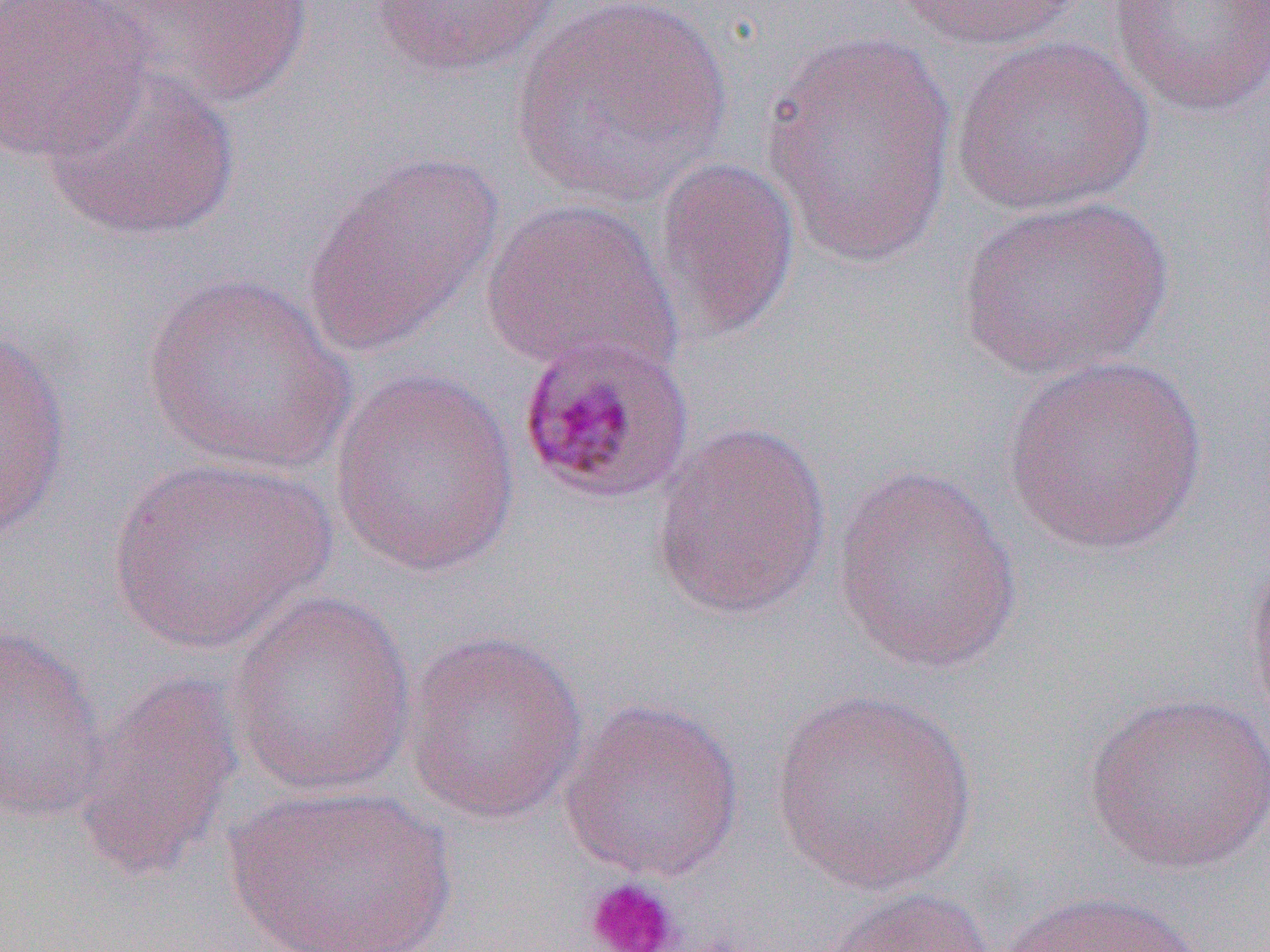
Summary:
  - Coordinate format: approximate bounding boxes as (x1,y1)-(x2,y2) corner pairs in pixels
  - Uninfected red blood cell locations: (0,0)-(153,165), (87,0)-(316,110), (369,0)-(566,78), (509,0)-(734,209), (886,0)-(1083,51), (1106,0)-(1270,118), (759,25)-(960,268), (951,35)-(1155,217), (42,59)-(241,243), (303,152)-(503,356), (651,154)-(802,344), (953,195)-(1175,382), (480,198)-(681,381), (140,274)-(357,476), (0,323)-(72,543), (1001,354)-(1211,557), (330,369)-(522,577), (650,418)-(833,621), (109,456)-(332,654), (831,463)-(1025,675), (1242,543)-(1270,736), (225,588)-(419,797), (0,623)-(109,823), (401,627)-(589,825), (71,671)-(245,886), (769,689)-(979,894), (1083,690)-(1270,876), (558,697)-(746,882), (225,783)-(456,952), (817,885)-(996,952), (992,890)-(1208,952)
  - Plasmodium malariae-infected red blood cell locations: (515,335)-(697,506)
  - Platelet locations: (582,876)-(683,952)
  - Slide-level diagnosis: Plasmodium malariae
  - Image size: 1270×952 pixels
  - Magnification: 1000x
  - Modality: light microscopy
  - Field of view: single
  - Preparation: thin blood film